Classify this cell by malaria status.
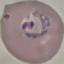

It is parasitized.

Summary:
  - Preparation: thin blood film
  - Capture: smartphone camera at the microscope eyepiece
  - Image type: automatically extracted cell patch, resized to 64 × 64 pixels
  - Stain: Giemsa